Give the extent of all uninfected red blood cells.
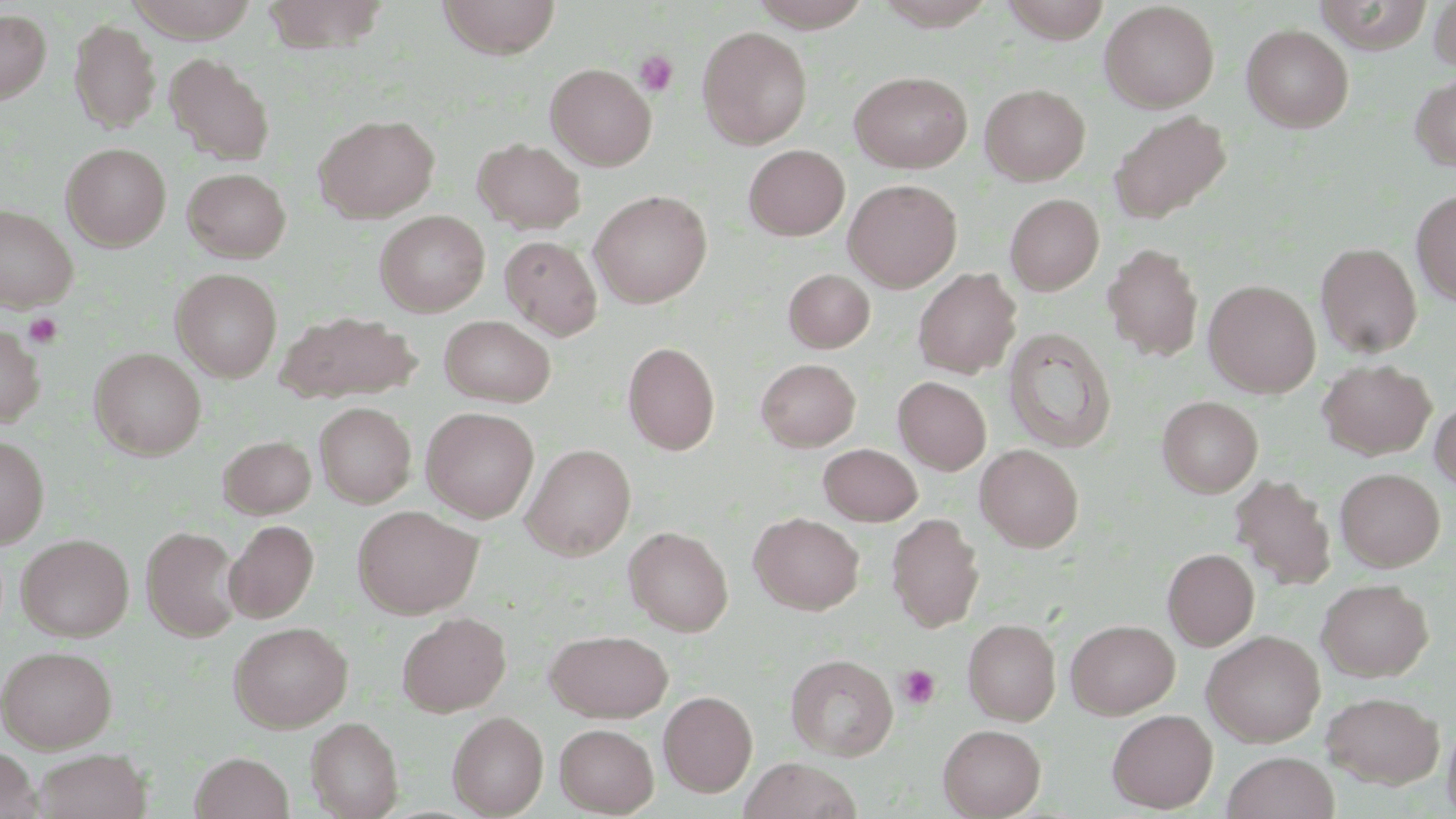

Approximate bounding boxes as named x1/y1/x2/y2 corners in pixels.
Uninfected red blood cells: (x1=126, y1=0, x2=260, y2=42), (x1=437, y1=0, x2=560, y2=57), (x1=748, y1=0, x2=874, y2=30), (x1=1001, y1=0, x2=1111, y2=43), (x1=1429, y1=0, x2=1456, y2=72), (x1=869, y1=2, x2=999, y2=29), (x1=1099, y1=2, x2=1219, y2=112), (x1=0, y1=9, x2=51, y2=104), (x1=70, y1=19, x2=161, y2=132), (x1=1241, y1=24, x2=1354, y2=132), (x1=697, y1=25, x2=812, y2=148), (x1=165, y1=53, x2=275, y2=165), (x1=546, y1=63, x2=656, y2=169), (x1=849, y1=70, x2=972, y2=173), (x1=1411, y1=72, x2=1456, y2=173), (x1=980, y1=83, x2=1090, y2=185), (x1=1108, y1=110, x2=1231, y2=225), (x1=316, y1=114, x2=440, y2=222), (x1=473, y1=138, x2=586, y2=234), (x1=61, y1=143, x2=171, y2=251), (x1=744, y1=145, x2=849, y2=240), (x1=182, y1=167, x2=290, y2=262), (x1=844, y1=179, x2=962, y2=291), (x1=589, y1=190, x2=712, y2=307), (x1=1411, y1=190, x2=1456, y2=305), (x1=1005, y1=193, x2=1104, y2=295), (x1=0, y1=205, x2=77, y2=312), (x1=375, y1=210, x2=490, y2=316), (x1=500, y1=235, x2=603, y2=341), (x1=1315, y1=242, x2=1422, y2=358), (x1=1103, y1=243, x2=1204, y2=362), (x1=171, y1=268, x2=283, y2=381), (x1=784, y1=268, x2=875, y2=353), (x1=913, y1=268, x2=1021, y2=379), (x1=1204, y1=280, x2=1321, y2=397), (x1=274, y1=310, x2=423, y2=403), (x1=439, y1=315, x2=556, y2=406), (x1=0, y1=322, x2=44, y2=428), (x1=1004, y1=327, x2=1116, y2=453), (x1=623, y1=341, x2=720, y2=455), (x1=89, y1=348, x2=207, y2=460), (x1=756, y1=358, x2=861, y2=451), (x1=1318, y1=359, x2=1436, y2=460), (x1=894, y1=377, x2=992, y2=475), (x1=1158, y1=396, x2=1262, y2=497), (x1=1430, y1=399, x2=1456, y2=495), (x1=315, y1=402, x2=416, y2=508), (x1=422, y1=407, x2=539, y2=522), (x1=0, y1=434, x2=49, y2=548), (x1=218, y1=435, x2=316, y2=519), (x1=522, y1=443, x2=636, y2=560), (x1=818, y1=443, x2=922, y2=526), (x1=975, y1=444, x2=1084, y2=552), (x1=1335, y1=468, x2=1445, y2=571), (x1=1231, y1=474, x2=1336, y2=590), (x1=352, y1=505, x2=483, y2=618), (x1=750, y1=512, x2=864, y2=614), (x1=887, y1=513, x2=984, y2=632), (x1=225, y1=520, x2=319, y2=623), (x1=141, y1=526, x2=243, y2=641), (x1=624, y1=526, x2=733, y2=636), (x1=16, y1=533, x2=134, y2=640), (x1=1162, y1=548, x2=1259, y2=650), (x1=1317, y1=579, x2=1433, y2=682), (x1=396, y1=611, x2=511, y2=716), (x1=963, y1=619, x2=1060, y2=724), (x1=1066, y1=619, x2=1179, y2=718), (x1=229, y1=621, x2=353, y2=733), (x1=948, y1=621, x2=1048, y2=819), (x1=545, y1=629, x2=673, y2=721), (x1=1202, y1=630, x2=1325, y2=747), (x1=0, y1=644, x2=118, y2=752), (x1=786, y1=654, x2=898, y2=760), (x1=658, y1=690, x2=757, y2=797), (x1=1321, y1=691, x2=1445, y2=789), (x1=1107, y1=709, x2=1218, y2=813), (x1=448, y1=711, x2=548, y2=817), (x1=1441, y1=715, x2=1456, y2=819), (x1=305, y1=717, x2=403, y2=818), (x1=555, y1=722, x2=659, y2=816), (x1=939, y1=724, x2=1046, y2=818), (x1=0, y1=745, x2=41, y2=819), (x1=33, y1=748, x2=151, y2=819), (x1=1222, y1=751, x2=1338, y2=819), (x1=190, y1=752, x2=293, y2=819), (x1=738, y1=757, x2=863, y2=819).

slide-level diagnosis = negative for blood parasites
image size = 1456×819 pixels
stain = May-Grünwald-Giemsa
field of view = one of a larger specimen
modality = light microscopy
platelet locations = approximate bounding boxes as named x1/y1/x2/y2 corners in pixels: (x1=634, y1=51, x2=678, y2=96), (x1=23, y1=313, x2=63, y2=348), (x1=896, y1=664, x2=941, y2=709)
magnification = 1000x
preparation = thin blood smear